Describe the morphology of the erythrocytes.
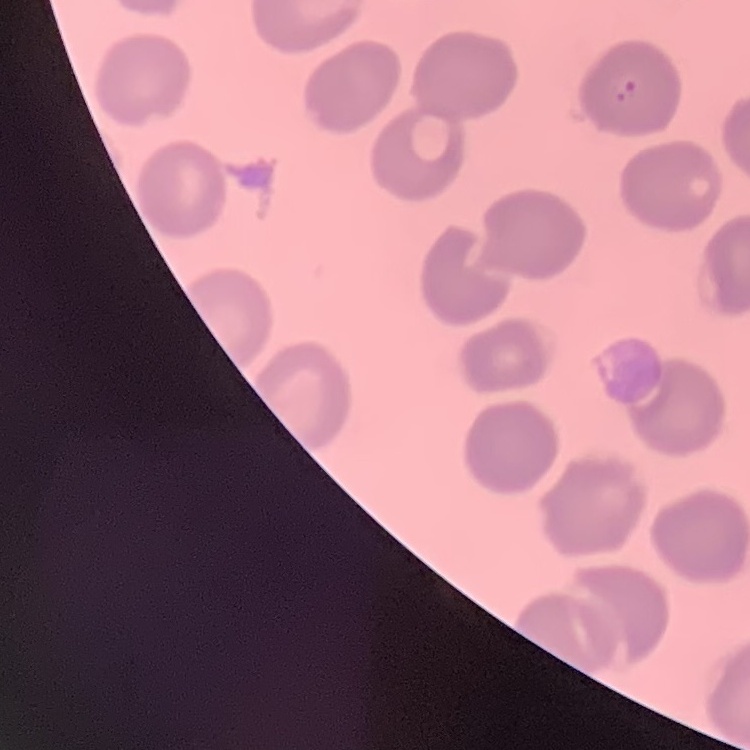
They show no rouleaux formation.

One tile cut from a larger photomicrograph. Thin blood smear. Stained with either Field's or Giemsa.